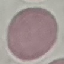 Result: negative for malaria parasites. Thin blood film. Cell patch, automatically extracted from a larger field of view and resized to 64 × 64 pixels. Giemsa stain. Acquired by smartphone through the microscope eyepiece.